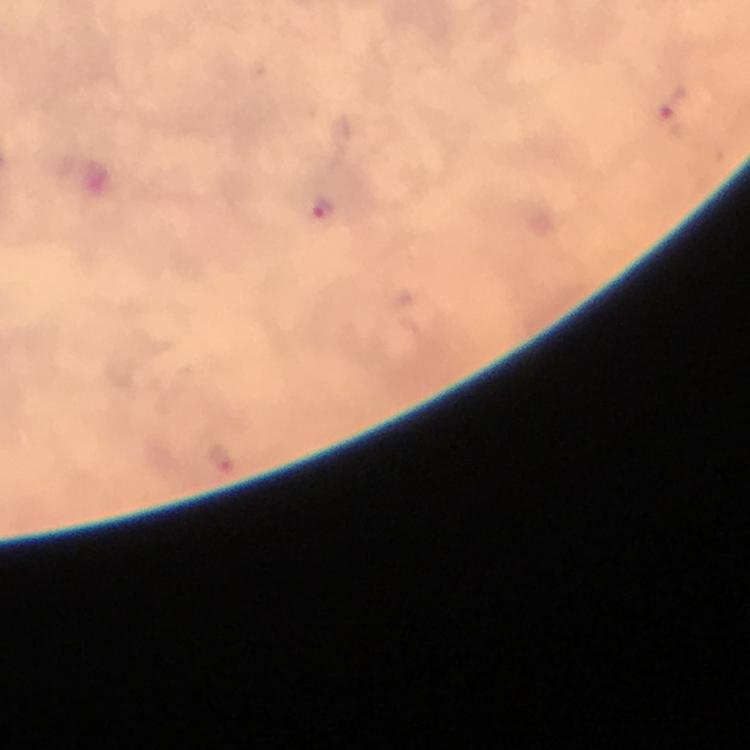

cropped from = a single field of view
image size = 750×750 pixels
magnification = 100x
context = from a malaria diagnostic workup
immersion oil = used
stain = Giemsa
Plasmodium parasite locations = approximate object centers, in pixels from the top-left corner: (x=673, y=110), (x=325, y=211)
capture = smartphone mounted on the microscope
preparation = thick blood film